Report the malaria status of this cell.
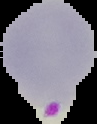
It is parasitized.

{
  "image_type": "cell region segmented out of the field of view; surrounding area masked to black",
  "preparation": "thin blood smear",
  "image_size": "97×124 pixels"
}